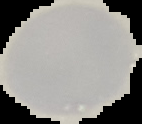

Summary:
  - Image size: 142×124 pixels
  - Image type: segmented cell region on a black background
  - Malaria status: uninfected
  - Preparation: thin blood film